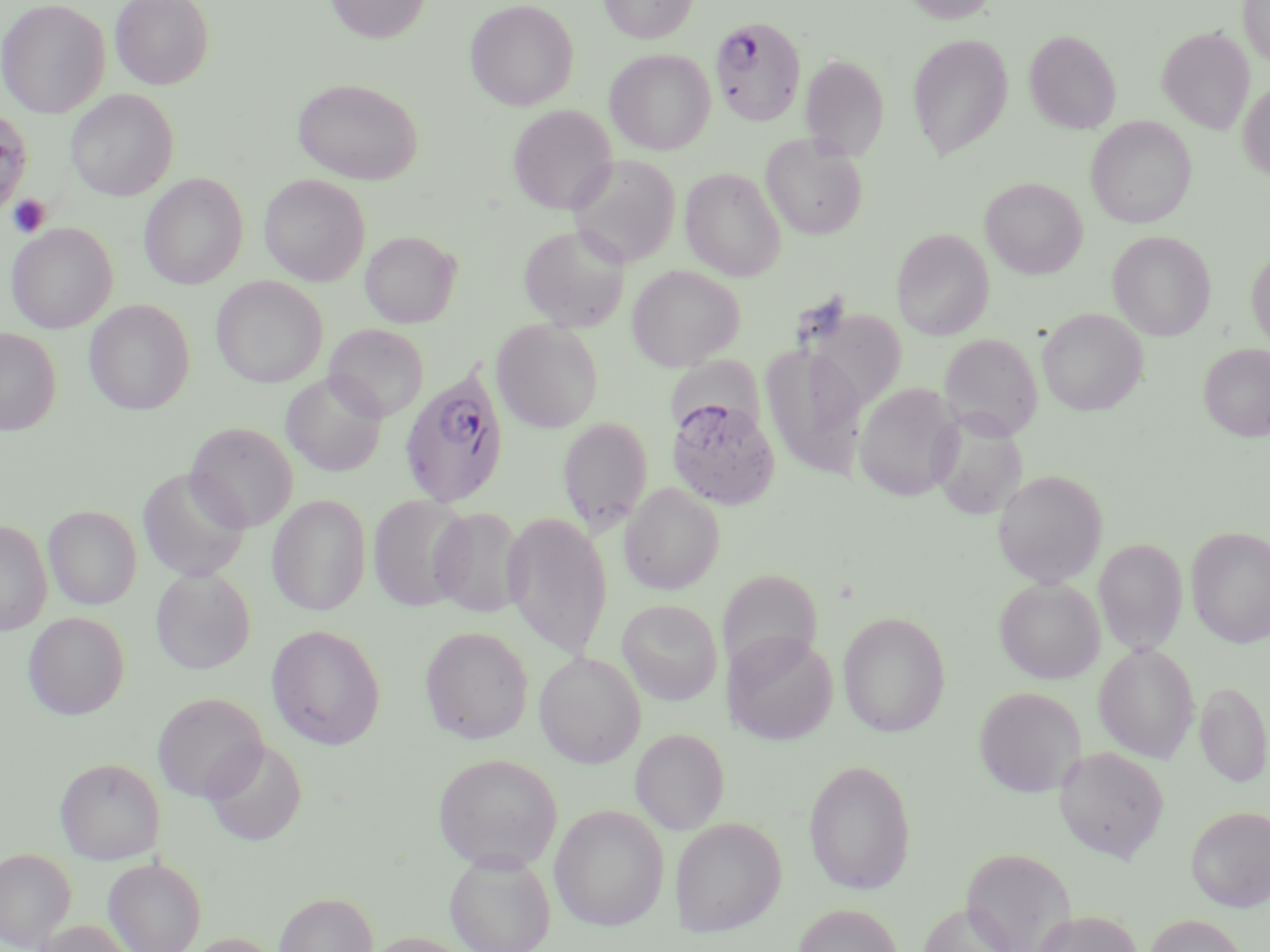

Approximate bounding boxes as named x1/y1/x2/y2 corners in pixels. Plasmodium falciparum-infected red blood cell locations: (x1=710, y1=16, x2=806, y2=126), (x1=0, y1=105, x2=34, y2=218), (x1=401, y1=369, x2=512, y2=511), (x1=666, y1=395, x2=781, y2=510). Uninfected red blood cell locations: (x1=110, y1=0, x2=214, y2=90), (x1=324, y1=0, x2=431, y2=43), (x1=465, y1=0, x2=579, y2=111), (x1=599, y1=0, x2=697, y2=43), (x1=900, y1=0, x2=999, y2=23), (x1=1238, y1=0, x2=1270, y2=67), (x1=0, y1=1, x2=110, y2=118), (x1=1158, y1=27, x2=1254, y2=135), (x1=1024, y1=30, x2=1122, y2=134), (x1=908, y1=33, x2=1013, y2=160), (x1=605, y1=48, x2=716, y2=155), (x1=799, y1=53, x2=889, y2=160), (x1=293, y1=79, x2=423, y2=184), (x1=1238, y1=80, x2=1270, y2=181), (x1=66, y1=89, x2=179, y2=201), (x1=508, y1=105, x2=618, y2=215), (x1=1086, y1=117, x2=1196, y2=228), (x1=761, y1=133, x2=868, y2=240), (x1=568, y1=154, x2=681, y2=267), (x1=681, y1=167, x2=787, y2=281), (x1=139, y1=174, x2=248, y2=289), (x1=259, y1=174, x2=370, y2=286), (x1=980, y1=177, x2=1087, y2=279), (x1=6, y1=222, x2=117, y2=333), (x1=519, y1=223, x2=631, y2=333), (x1=892, y1=228, x2=994, y2=340), (x1=360, y1=230, x2=461, y2=328), (x1=1108, y1=230, x2=1216, y2=340), (x1=1247, y1=245, x2=1270, y2=354), (x1=627, y1=264, x2=745, y2=371), (x1=211, y1=276, x2=328, y2=387), (x1=84, y1=300, x2=195, y2=415), (x1=804, y1=308, x2=906, y2=414), (x1=1037, y1=308, x2=1147, y2=416), (x1=492, y1=319, x2=604, y2=433), (x1=324, y1=323, x2=429, y2=421), (x1=0, y1=328, x2=61, y2=436), (x1=939, y1=333, x2=1043, y2=440), (x1=1198, y1=343, x2=1270, y2=441), (x1=762, y1=344, x2=869, y2=480), (x1=281, y1=372, x2=387, y2=476), (x1=854, y1=384, x2=964, y2=501), (x1=931, y1=414, x2=1028, y2=520), (x1=558, y1=417, x2=653, y2=530), (x1=186, y1=421, x2=298, y2=532), (x1=137, y1=467, x2=252, y2=582), (x1=992, y1=469, x2=1108, y2=587), (x1=619, y1=482, x2=725, y2=594), (x1=268, y1=494, x2=371, y2=616), (x1=369, y1=494, x2=474, y2=611), (x1=44, y1=505, x2=142, y2=610), (x1=430, y1=506, x2=527, y2=617), (x1=502, y1=512, x2=613, y2=660), (x1=0, y1=519, x2=52, y2=636), (x1=1186, y1=527, x2=1270, y2=648), (x1=1093, y1=538, x2=1188, y2=655), (x1=151, y1=567, x2=256, y2=674), (x1=717, y1=568, x2=823, y2=678), (x1=994, y1=577, x2=1105, y2=684), (x1=617, y1=600, x2=723, y2=706), (x1=838, y1=611, x2=951, y2=737), (x1=24, y1=612, x2=129, y2=719), (x1=266, y1=624, x2=386, y2=750), (x1=420, y1=626, x2=533, y2=744), (x1=724, y1=630, x2=838, y2=745), (x1=1093, y1=641, x2=1199, y2=763), (x1=534, y1=652, x2=646, y2=768), (x1=1195, y1=680, x2=1270, y2=787), (x1=974, y1=687, x2=1086, y2=797), (x1=152, y1=692, x2=268, y2=802), (x1=630, y1=728, x2=729, y2=835), (x1=203, y1=738, x2=307, y2=846), (x1=1053, y1=746, x2=1170, y2=862), (x1=432, y1=753, x2=563, y2=872), (x1=55, y1=757, x2=165, y2=864), (x1=802, y1=758, x2=917, y2=895), (x1=549, y1=804, x2=669, y2=932), (x1=1185, y1=805, x2=1270, y2=910), (x1=670, y1=817, x2=785, y2=936), (x1=0, y1=847, x2=77, y2=950), (x1=961, y1=847, x2=1077, y2=952), (x1=444, y1=851, x2=556, y2=952), (x1=103, y1=857, x2=207, y2=952), (x1=275, y1=891, x2=378, y2=952), (x1=919, y1=902, x2=1027, y2=952), (x1=793, y1=903, x2=902, y2=952), (x1=1032, y1=910, x2=1143, y2=952), (x1=1143, y1=914, x2=1250, y2=951), (x1=34, y1=919, x2=135, y2=952), (x1=361, y1=932, x2=478, y2=952), (x1=181, y1=933, x2=285, y2=952). Platelet locations: (x1=9, y1=194, x2=51, y2=237). Slide-level diagnosis: Plasmodium falciparum. May-Grünwald-Giemsa-stained preparation. One field of a larger specimen. Light microscopy. Captured at 1000x magnification. Image is 1270×952 pixels. Thin blood smear.